Point out each leukocyte.
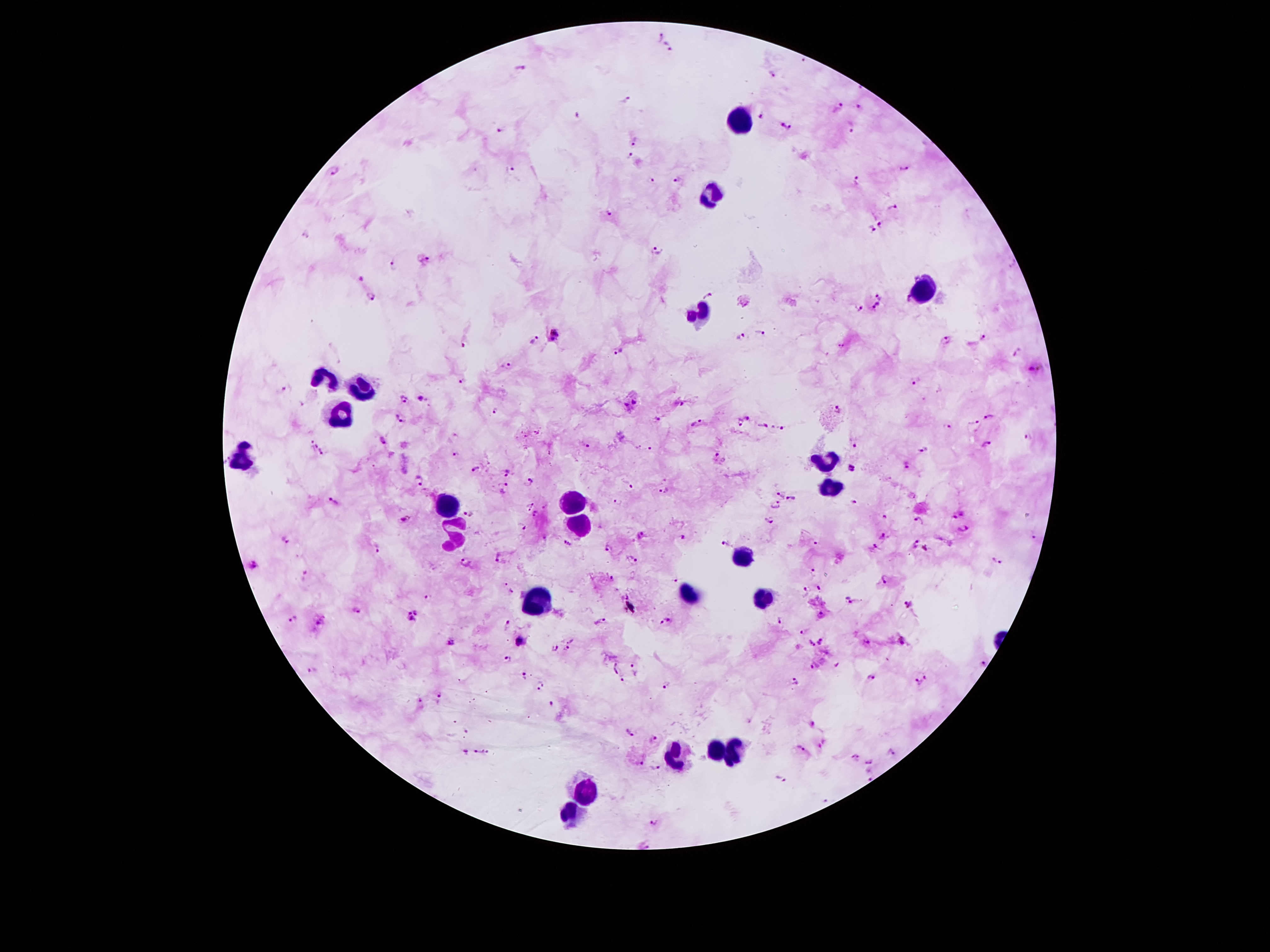
Approximate centers as {x, y} in pixels.
Leukocytes: {737, 119}, {715, 197}, {922, 291}, {702, 313}, {323, 380}, {358, 392}, {339, 413}, {243, 458}, {823, 463}, {827, 487}, {570, 503}, {449, 506}, {579, 522}, {455, 534}, {741, 556}, {688, 595}, {764, 599}, {540, 600}, {712, 748}, {735, 751}, {675, 754}, {584, 790}, {570, 813}.

Summary:
  - Plasmodium parasite locations: {659, 36}, {669, 46}, {803, 62}, {520, 69}, {772, 75}, {628, 100}, {836, 108}, {861, 108}, {577, 115}, {763, 116}, {851, 125}, {787, 127}, {500, 131}, {635, 141}, {629, 157}, {903, 168}, {334, 169}, {512, 170}, {679, 181}, {856, 181}, {652, 182}, {891, 207}, {608, 214}, {881, 224}, {871, 229}, {306, 234}, {658, 251}, {428, 259}, {393, 265}, {360, 278}, {708, 295}, {372, 297}, {879, 297}, {876, 306}, {859, 309}, {555, 332}, {761, 333}, {985, 337}, {741, 338}, {535, 340}, {553, 340}, {944, 342}, {464, 343}, {842, 345}, {619, 350}, {1016, 353}, {510, 367}, {1033, 368}, {463, 381}, {915, 381}, {285, 390}, {407, 399}, {422, 400}, {635, 401}, {679, 404}, {624, 406}, {495, 410}, {839, 410}, {989, 416}, {747, 418}, {400, 419}, {657, 421}, {972, 422}, {697, 423}, {739, 424}, {762, 426}, {781, 427}, {947, 428}, {1028, 437}, {382, 441}, {312, 444}, {854, 445}, {986, 445}, {585, 446}, {650, 450}, {924, 450}, {322, 454}, {456, 455}, {715, 457}, {907, 464}, {853, 468}, {476, 469}, {507, 472}, {419, 480}, {531, 481}, {627, 484}, {503, 485}, {664, 491}, {778, 495}, {793, 500}, {335, 502}, {853, 502}, {618, 503}, {530, 504}, {545, 505}, {774, 507}, {468, 513}, {536, 514}, {959, 515}, {884, 517}, {406, 519}, {919, 521}, {770, 522}, {522, 525}, {964, 529}, {642, 534}, {883, 536}, {1035, 537}, {684, 538}, {286, 539}, {726, 543}, {816, 543}, {913, 543}, {567, 544}, {608, 548}, {376, 549}, {875, 549}, {926, 549}, {498, 558}, {633, 558}, {995, 560}, {465, 562}, {252, 567}, {814, 572}, {609, 579}, {674, 579}, {885, 579}, {506, 584}, {820, 587}, {512, 591}, {803, 592}, {427, 596}, {846, 600}, {910, 604}, {356, 609}, {416, 611}, {821, 615}, {410, 618}, {779, 619}, {293, 620}, {321, 621}, {666, 621}, {600, 622}, {508, 625}, {806, 630}, {821, 639}, {902, 640}, {521, 641}, {450, 642}, {866, 642}, {812, 644}, {571, 646}, {554, 649}, {506, 659}, {984, 664}, {814, 666}, {634, 669}, {312, 671}, {522, 677}, {873, 677}, {622, 679}, {920, 680}, {794, 682}, {665, 684}, {539, 688}, {439, 695}, {419, 703}, {549, 705}, {465, 730}, {632, 732}, {654, 739}, {799, 747}, {891, 750}, {466, 753}, {478, 754}, {855, 756}, {639, 761}, {869, 762}, {656, 768}, {868, 776}, {780, 780}, {655, 822}, {644, 845}
  - Capture: smartphone camera through the microscope eyepiece
  - Field of view: single
  - Stain: Giemsa
  - Magnification: 100x
  - Image size: 1270×952 pixels
  - Patient malaria status: positive for Plasmodium falciparum
  - Preparation: thick blood smear